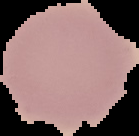 Result: no malaria parasites detected. Image is 139×136 pixels. Cell region segmented out of the field of view; the surrounding area is masked to black. From a thin blood film.